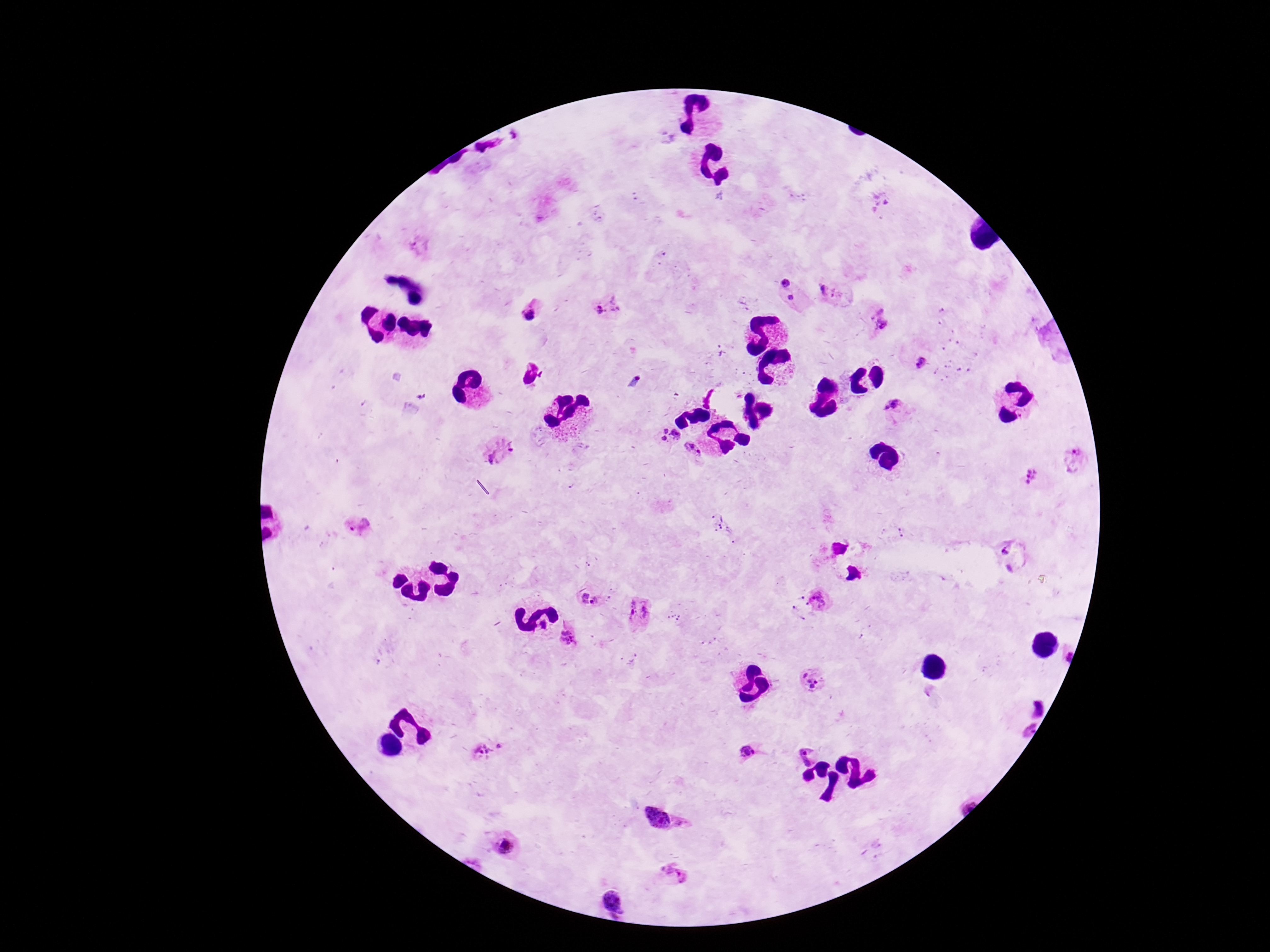

Approximate centers as {x, y} in pixels.
Summary:
  - Plasmodium parasite locations: {791, 292}, {835, 292}, {610, 309}, {529, 311}, {883, 320}, {926, 367}, {897, 411}, {669, 436}, {501, 450}, {694, 450}, {1075, 460}, {1032, 477}, {358, 529}, {1012, 560}, {589, 600}, {821, 601}, {640, 614}, {568, 639}, {809, 681}, {750, 751}, {486, 752}, {663, 821}, {505, 847}, {672, 873}, {614, 901}
  - Stain: Giemsa
  - Field of view: single
  - Magnification: 100x
  - Image size: 1270×952 pixels
  - Preparation: thick peripheral-blood smear
  - Capture: smartphone camera through the microscope eyepiece
  - Patient malaria status: positive